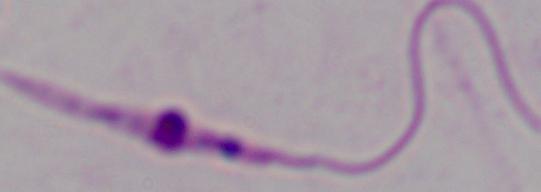
{
  "identification": "Leishmania",
  "magnification": "1000x",
  "modality": "photomicrograph"
}